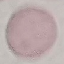
Summary:
  - Malaria status: uninfected
  - Capture: smartphone through the microscope eyepiece
  - Stain: Giemsa
  - Preparation: thin blood film
  - Image type: cell patch, automatically extracted from a larger field of view and resized to 64 × 64 pixels